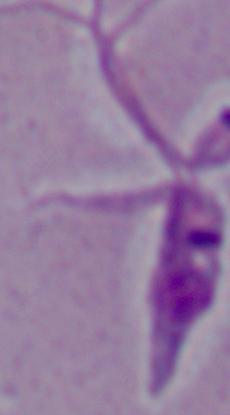
Micrograph. 1000x magnification. A Leishmania parasite is seen.